State the blood parasite species.
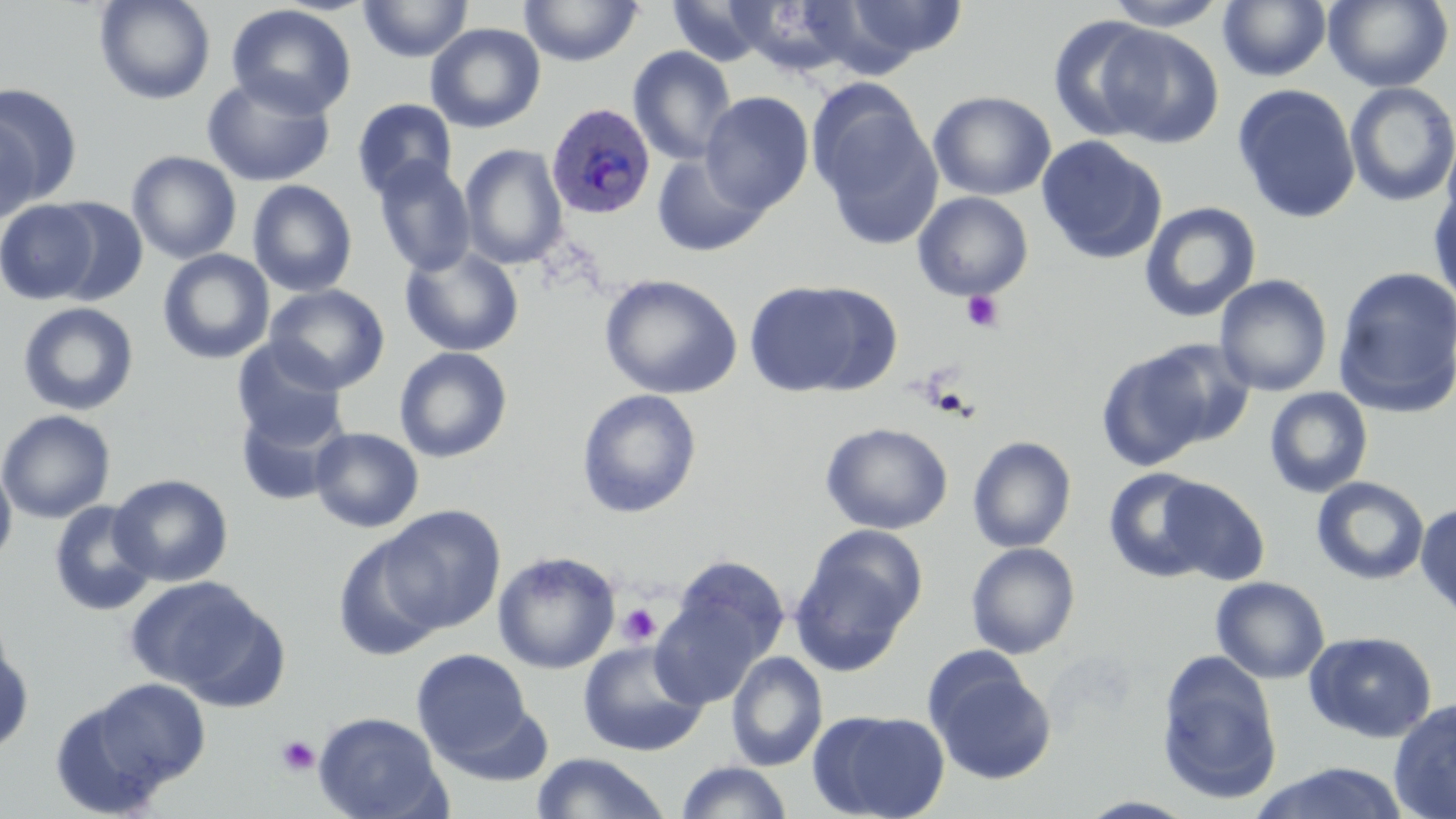
Plasmodium ovale.

Approximate bounding boxes as [x1, y1, x2, y2] in pixels. Uninfected red blood cell locations: [93, 0, 217, 105], [358, 0, 473, 63], [519, 0, 643, 67], [1101, 0, 1228, 30], [1324, 0, 1454, 92], [667, 1, 772, 67], [825, 1, 968, 67], [1218, 1, 1332, 82], [225, 4, 357, 119], [1047, 16, 1167, 141], [425, 23, 546, 133], [1096, 25, 1224, 147], [627, 45, 738, 166], [201, 75, 336, 187], [1344, 82, 1456, 208], [1, 84, 83, 205], [1232, 84, 1361, 224], [811, 90, 942, 249], [928, 90, 1056, 201], [700, 91, 814, 214], [351, 98, 458, 200], [1, 114, 42, 225], [1440, 128, 1456, 232], [1036, 135, 1167, 265], [459, 143, 568, 270], [126, 150, 242, 264], [651, 153, 770, 257], [371, 156, 475, 277], [247, 179, 358, 297], [1428, 183, 1456, 309], [913, 191, 1033, 300], [46, 197, 149, 306], [1, 200, 101, 305], [1139, 201, 1261, 323], [399, 246, 525, 357], [157, 249, 275, 364], [1333, 265, 1456, 417], [599, 274, 743, 400], [1213, 275, 1333, 396], [743, 279, 895, 398], [264, 284, 390, 394], [17, 302, 140, 416], [231, 339, 348, 450], [1096, 343, 1237, 469], [394, 346, 513, 463], [1264, 387, 1374, 498], [576, 388, 702, 519], [235, 402, 346, 506], [0, 409, 116, 524], [821, 422, 953, 534], [309, 427, 424, 533], [967, 436, 1076, 553], [0, 459, 17, 570], [1103, 467, 1216, 582], [109, 473, 233, 587], [1157, 476, 1270, 586], [1311, 476, 1430, 585], [49, 500, 158, 617], [1415, 502, 1456, 622], [380, 506, 504, 634], [790, 526, 926, 672], [332, 535, 446, 662], [966, 542, 1080, 659], [493, 551, 620, 674], [667, 554, 790, 670], [125, 576, 279, 702], [1211, 576, 1330, 684], [650, 591, 769, 710], [1304, 630, 1438, 743], [0, 633, 35, 757], [578, 640, 708, 756], [411, 649, 533, 763], [1156, 650, 1284, 806], [726, 651, 827, 771], [926, 657, 1057, 785], [81, 678, 211, 793], [1388, 698, 1456, 818], [810, 709, 950, 819], [313, 711, 449, 819], [531, 752, 671, 818], [673, 761, 795, 818], [1248, 762, 1411, 819], [1078, 796, 1199, 818]. Plasmodium ovale-infected red blood cell locations: [546, 101, 657, 219]. Platelet locations: [961, 290, 1004, 332], [927, 387, 974, 419], [617, 603, 660, 646], [276, 735, 320, 776]. Single field of view. Image is 1456×819 pixels. Optical microscopy. Thin blood smear. Captured at 1000x magnification. May-Grünwald-Giemsa stain.